Describe the morphology of the red blood cells.
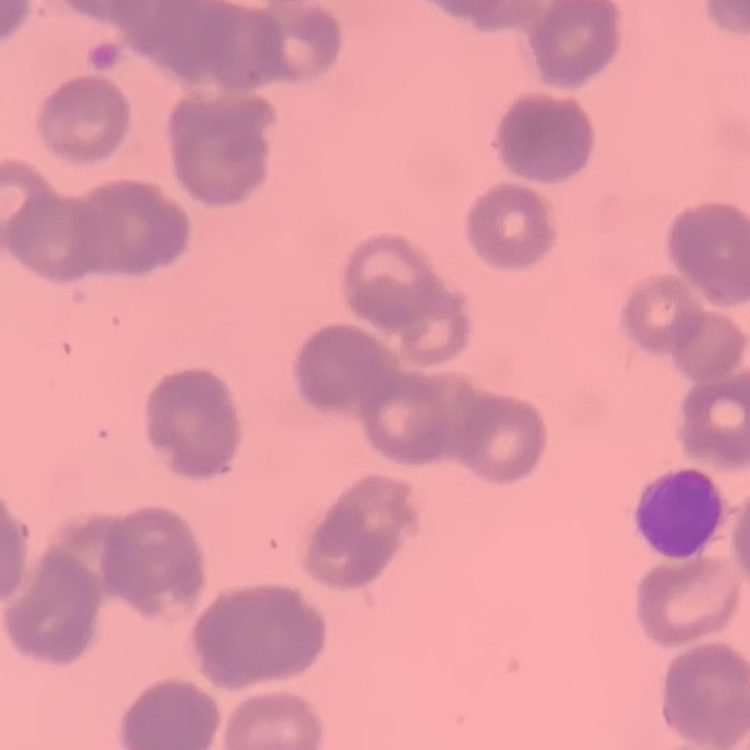
They show rouleaux formation.

Summary:
  - Image type: square crop of a larger photomicrograph
  - Stain: Field's or Giemsa
  - Preparation: thin blood smear